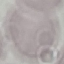
Summary:
  - Result: negative for malaria parasites
  - Preparation: thin blood smear
  - Image type: automatically extracted cell patch, resized to 64 × 64 pixels
  - Stain: Giemsa
  - Capture: smartphone through the microscope eyepiece